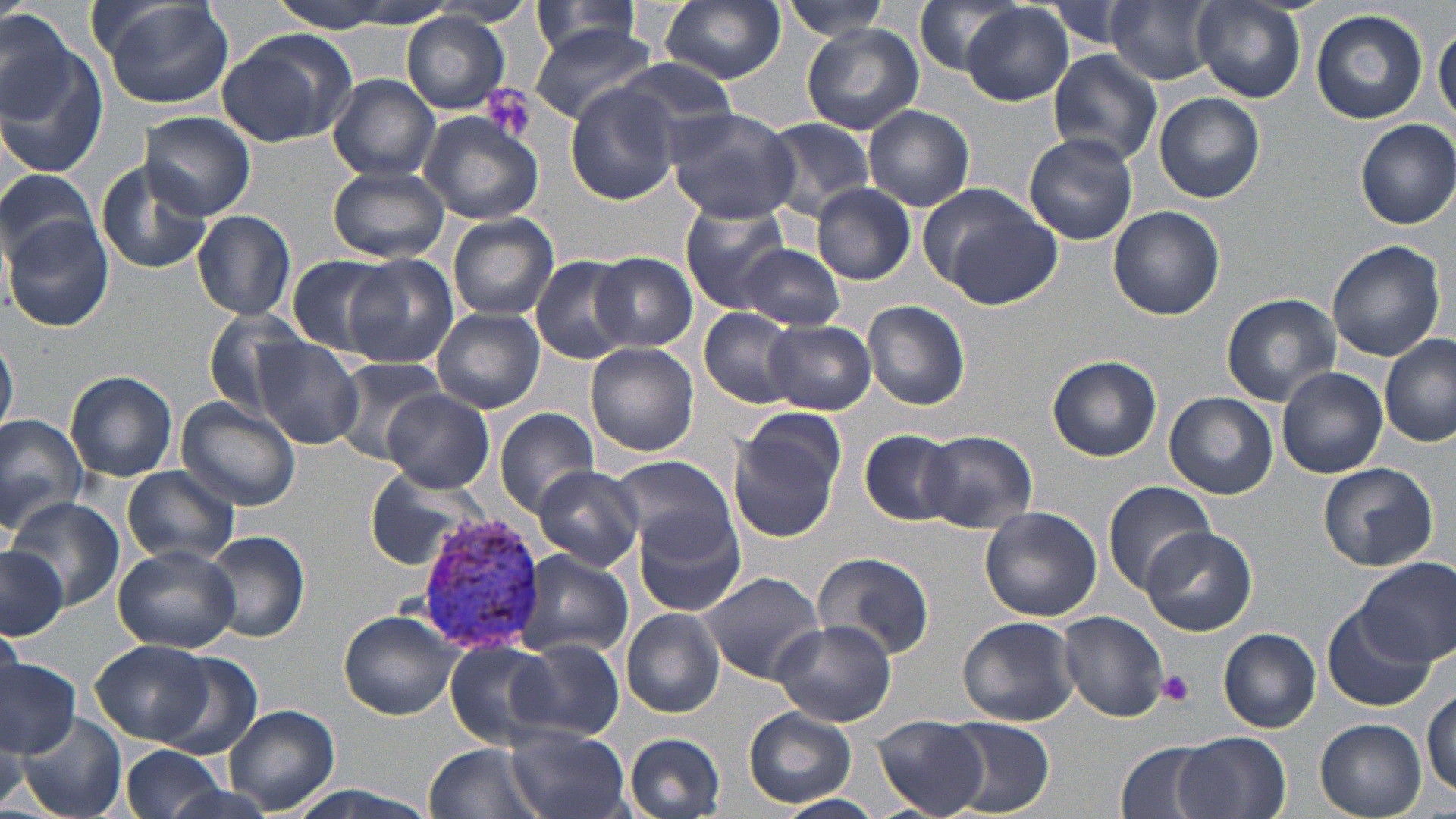
slide_level_diagnosis: Plasmodium vivax
preparation: thin blood film
modality: light microscopy
plasmodium_vivax_infected_red_blood_cell_locations: 'approximate bounding boxes as named x1/y1/x2/y2 corners in pixels: (x1=413, y1=511, x2=547, y2=653)'
field_of_view: one of a larger specimen
stain: May-Grünwald-Giemsa
uninfected_red_blood_cell_locations: 'approximate bounding boxes as named x1/y1/x2/y2 corners in pixels: (x1=94, y1=0, x2=235, y2=109), (x1=267, y1=0, x2=435, y2=32), (x1=661, y1=0, x2=786, y2=83), (x1=910, y1=0, x2=1032, y2=76), (x1=1192, y1=0, x2=1305, y2=101), (x1=1042, y1=1, x2=1142, y2=50), (x1=436, y1=2, x2=536, y2=26), (x1=780, y1=2, x2=891, y2=40), (x1=958, y1=2, x2=1076, y2=106), (x1=1106, y1=2, x2=1219, y2=84), (x1=525, y1=4, x2=651, y2=60), (x1=0, y1=9, x2=102, y2=169), (x1=1311, y1=9, x2=1428, y2=123), (x1=403, y1=13, x2=510, y2=112), (x1=1434, y1=21, x2=1456, y2=127), (x1=529, y1=22, x2=658, y2=125), (x1=802, y1=24, x2=923, y2=135), (x1=217, y1=29, x2=359, y2=147), (x1=1046, y1=49, x2=1163, y2=168), (x1=606, y1=60, x2=738, y2=153), (x1=328, y1=74, x2=441, y2=182), (x1=567, y1=88, x2=682, y2=204), (x1=1154, y1=92, x2=1264, y2=203), (x1=862, y1=105, x2=975, y2=211), (x1=666, y1=108, x2=802, y2=223), (x1=138, y1=110, x2=254, y2=221), (x1=419, y1=111, x2=545, y2=225), (x1=759, y1=118, x2=878, y2=218), (x1=1355, y1=119, x2=1456, y2=229), (x1=1024, y1=133, x2=1139, y2=244), (x1=96, y1=162, x2=214, y2=274), (x1=327, y1=164, x2=449, y2=263), (x1=0, y1=167, x2=99, y2=265), (x1=812, y1=185, x2=916, y2=285), (x1=922, y1=186, x2=1064, y2=307), (x1=788, y1=187, x2=903, y2=363), (x1=680, y1=198, x2=795, y2=310), (x1=1107, y1=206, x2=1224, y2=320), (x1=192, y1=209, x2=296, y2=320), (x1=446, y1=212, x2=559, y2=320), (x1=3, y1=217, x2=114, y2=332), (x1=1326, y1=241, x2=1448, y2=360), (x1=737, y1=243, x2=844, y2=330), (x1=592, y1=252, x2=698, y2=351), (x1=343, y1=254, x2=456, y2=368), (x1=284, y1=255, x2=402, y2=356), (x1=530, y1=255, x2=632, y2=364), (x1=1220, y1=293, x2=1340, y2=405), (x1=863, y1=299, x2=970, y2=411), (x1=433, y1=307, x2=545, y2=413), (x1=203, y1=308, x2=312, y2=416), (x1=699, y1=308, x2=802, y2=409), (x1=764, y1=320, x2=876, y2=413), (x1=1380, y1=335, x2=1456, y2=447), (x1=0, y1=336, x2=18, y2=435), (x1=252, y1=338, x2=364, y2=449), (x1=585, y1=343, x2=698, y2=457), (x1=1046, y1=355, x2=1162, y2=461), (x1=330, y1=358, x2=447, y2=464), (x1=1278, y1=366, x2=1388, y2=478), (x1=67, y1=369, x2=179, y2=483), (x1=381, y1=389, x2=494, y2=492), (x1=1165, y1=394, x2=1277, y2=499), (x1=177, y1=397, x2=302, y2=512), (x1=495, y1=407, x2=600, y2=519), (x1=729, y1=410, x2=847, y2=542), (x1=0, y1=413, x2=89, y2=536), (x1=860, y1=429, x2=962, y2=524), (x1=918, y1=431, x2=1039, y2=533), (x1=610, y1=454, x2=735, y2=555), (x1=1317, y1=462, x2=1440, y2=571), (x1=533, y1=464, x2=645, y2=571), (x1=121, y1=465, x2=241, y2=566), (x1=366, y1=469, x2=483, y2=570), (x1=1103, y1=479, x2=1216, y2=593), (x1=8, y1=496, x2=124, y2=609), (x1=980, y1=506, x2=1102, y2=621), (x1=635, y1=510, x2=748, y2=618), (x1=1140, y1=527, x2=1256, y2=636), (x1=201, y1=530, x2=310, y2=641), (x1=113, y1=543, x2=241, y2=653), (x1=0, y1=548, x2=67, y2=638), (x1=514, y1=550, x2=634, y2=659), (x1=812, y1=551, x2=936, y2=662), (x1=1357, y1=557, x2=1455, y2=665), (x1=694, y1=570, x2=827, y2=684), (x1=1324, y1=604, x2=1434, y2=712), (x1=621, y1=609, x2=725, y2=718), (x1=339, y1=610, x2=460, y2=719), (x1=1059, y1=611, x2=1169, y2=722), (x1=957, y1=616, x2=1080, y2=726), (x1=772, y1=619, x2=895, y2=728), (x1=0, y1=622, x2=25, y2=699), (x1=1218, y1=628, x2=1321, y2=732), (x1=510, y1=636, x2=624, y2=740), (x1=92, y1=639, x2=215, y2=745), (x1=444, y1=641, x2=554, y2=747), (x1=159, y1=654, x2=262, y2=758), (x1=0, y1=656, x2=80, y2=759), (x1=1423, y1=686, x2=1456, y2=797), (x1=226, y1=704, x2=340, y2=817), (x1=744, y1=708, x2=857, y2=807), (x1=12, y1=712, x2=127, y2=818), (x1=874, y1=715, x2=989, y2=818), (x1=944, y1=718, x2=1056, y2=816), (x1=1315, y1=719, x2=1428, y2=817), (x1=507, y1=727, x2=633, y2=819), (x1=0, y1=732, x2=28, y2=816), (x1=624, y1=732, x2=726, y2=818), (x1=1174, y1=733, x2=1292, y2=819), (x1=1116, y1=740, x2=1226, y2=819), (x1=425, y1=741, x2=544, y2=819), (x1=118, y1=744, x2=231, y2=819), (x1=275, y1=785, x2=448, y2=819), (x1=775, y1=794, x2=885, y2=818)'
platelet_locations: 'approximate bounding boxes as named x1/y1/x2/y2 corners in pixels: (x1=480, y1=84, x2=535, y2=143), (x1=1157, y1=668, x2=1196, y2=707)'
magnification: 1000x
image_size: 1456×819 pixels